Evaluate for malaria.
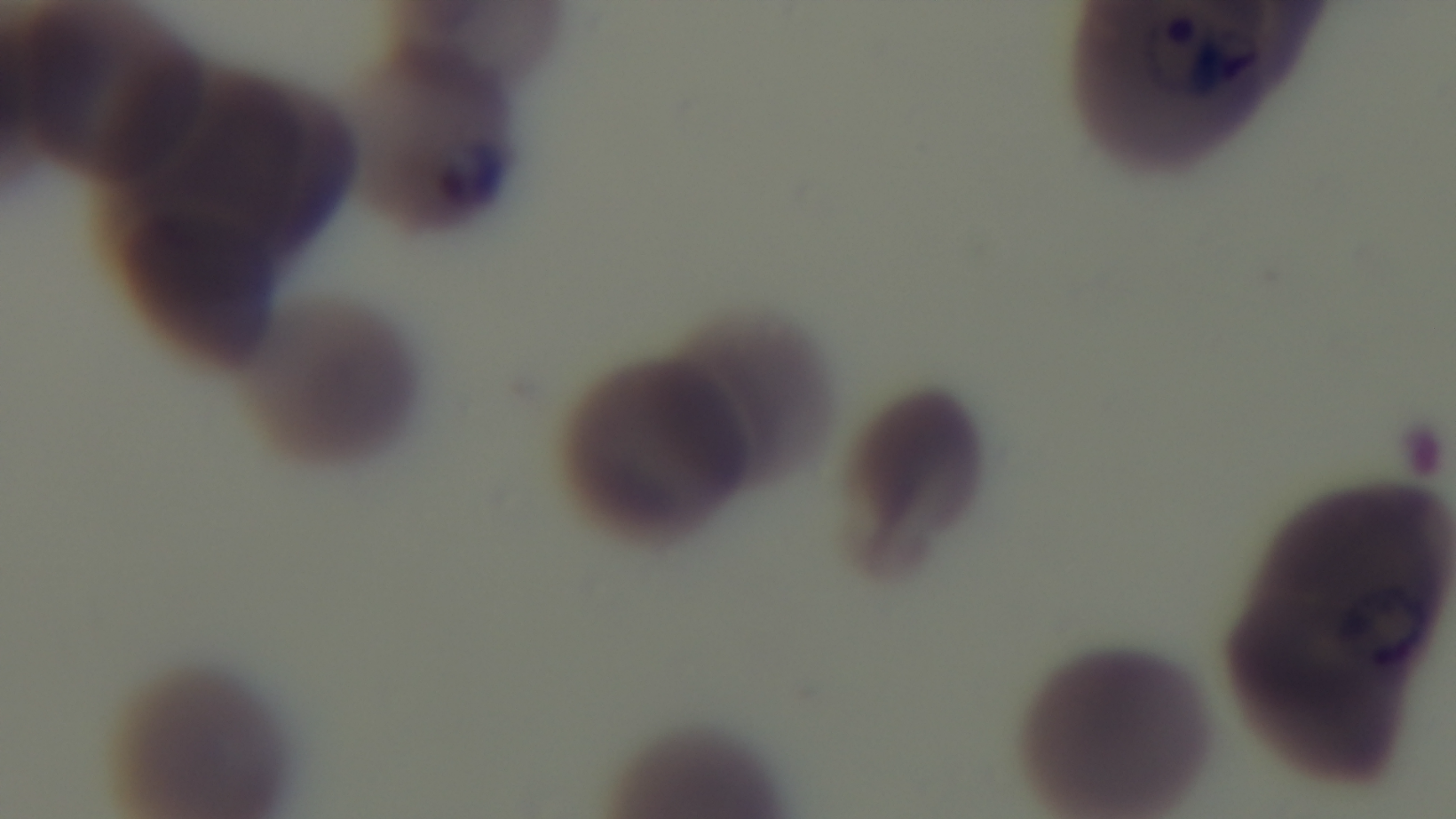
It is infected.

Giemsa-stained. Light microscopy. Preparation: thin smear. Captured with a mounted 4K digital camera. 100x oil-immersion objective. One field from the slide.